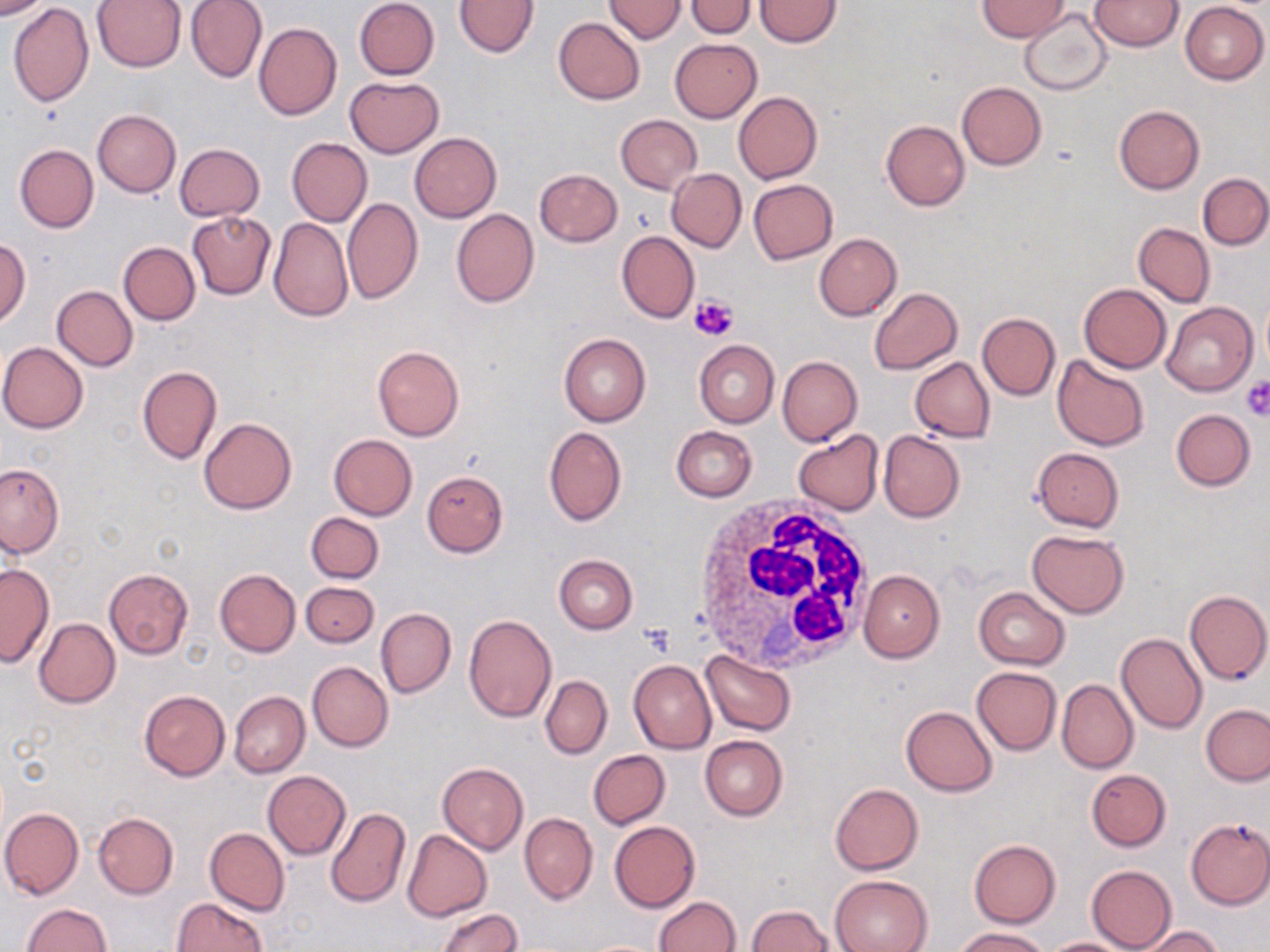
Summary:
  - Coordinate format: approximate bounding boxes as (x1,y1)-(x2,y2) corner pairs in pixels
  - Uninfected red blood cell locations: (0,0)-(52,19), (92,0)-(186,71), (186,0)-(267,83), (353,0)-(440,80), (455,0)-(540,57), (604,0)-(685,43), (754,0)-(842,46), (978,0)-(1071,41), (1089,1)-(1184,52), (685,2)-(757,37), (1180,2)-(1269,85), (9,3)-(94,107), (1019,8)-(1113,95), (553,17)-(646,104), (253,22)-(341,120), (670,39)-(761,121), (346,76)-(444,158), (957,82)-(1047,170), (734,91)-(822,184), (1113,105)-(1205,194), (92,110)-(181,197), (615,115)-(702,194), (881,120)-(970,211), (409,133)-(501,222), (287,138)-(371,227), (14,144)-(99,232), (174,144)-(265,222), (533,168)-(622,247), (667,168)-(746,252), (1198,173)-(1269,249), (748,178)-(837,263), (342,197)-(423,304), (451,208)-(539,308), (186,211)-(276,299), (268,216)-(353,321), (1133,222)-(1215,308), (616,231)-(700,322), (814,233)-(902,320), (0,237)-(30,327), (118,241)-(200,325), (1079,283)-(1171,373), (52,286)-(138,371), (869,287)-(963,374), (1259,295)-(1270,371), (1163,302)-(1258,396), (977,312)-(1060,400), (558,334)-(651,426), (694,340)-(779,429), (1,341)-(88,433), (372,345)-(464,441), (1052,355)-(1150,451), (777,356)-(863,446), (911,357)-(994,442), (137,366)-(222,464), (1170,409)-(1255,491), (200,417)-(297,513), (544,425)-(626,526), (671,426)-(758,502), (793,430)-(884,515), (877,430)-(965,523), (329,434)-(418,520), (1032,447)-(1124,532), (0,462)-(64,558), (421,470)-(508,557), (305,512)-(384,583), (1027,530)-(1129,617), (553,554)-(639,634), (0,562)-(52,668), (103,568)-(193,661), (215,569)-(300,657), (858,570)-(946,662), (301,582)-(379,648), (974,587)-(1071,669), (1184,589)-(1270,685), (376,608)-(456,698), (463,614)-(557,722), (33,619)-(121,708), (1116,632)-(1208,735), (701,650)-(797,736), (629,659)-(716,753), (307,661)-(393,752), (972,666)-(1061,754), (540,675)-(611,759), (978,676)-(1133,767), (1057,678)-(1138,773), (138,689)-(231,781), (229,691)-(309,778), (1202,704)-(1270,786), (900,706)-(998,796), (700,735)-(788,820), (588,750)-(670,829), (437,761)-(527,854), (1086,769)-(1172,851), (263,771)-(351,859), (830,783)-(923,875), (325,806)-(409,908), (1,807)-(84,898), (93,812)-(178,898), (520,812)-(597,904), (1184,817)-(1270,909), (609,821)-(700,913), (204,827)-(290,916), (402,830)-(492,921), (969,840)-(1061,928), (1086,864)-(1176,952), (830,874)-(933,952), (653,896)-(741,952), (172,897)-(267,951), (21,903)-(112,952), (745,905)-(835,951), (434,907)-(522,952), (1138,926)-(1226,952), (955,928)-(1046,951), (1039,937)-(1139,951)
  - White blood cell locations: (694,496)-(881,674)
  - Platelet locations: (690,292)-(739,343), (1240,375)-(1270,420), (638,622)-(677,655)
  - Slide-level diagnosis: no evidence of blood parasites
  - Stain: May-Grünwald-Giemsa
  - Field of view: single
  - Image size: 1270×952 pixels
  - Preparation: thin blood smear
  - Modality: light microscopy
  - Magnification: 1000x